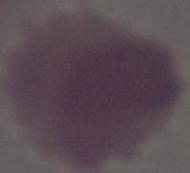
Summary:
  - Identification: erythrocyte
  - Magnification: 1000x
  - Modality: micrograph